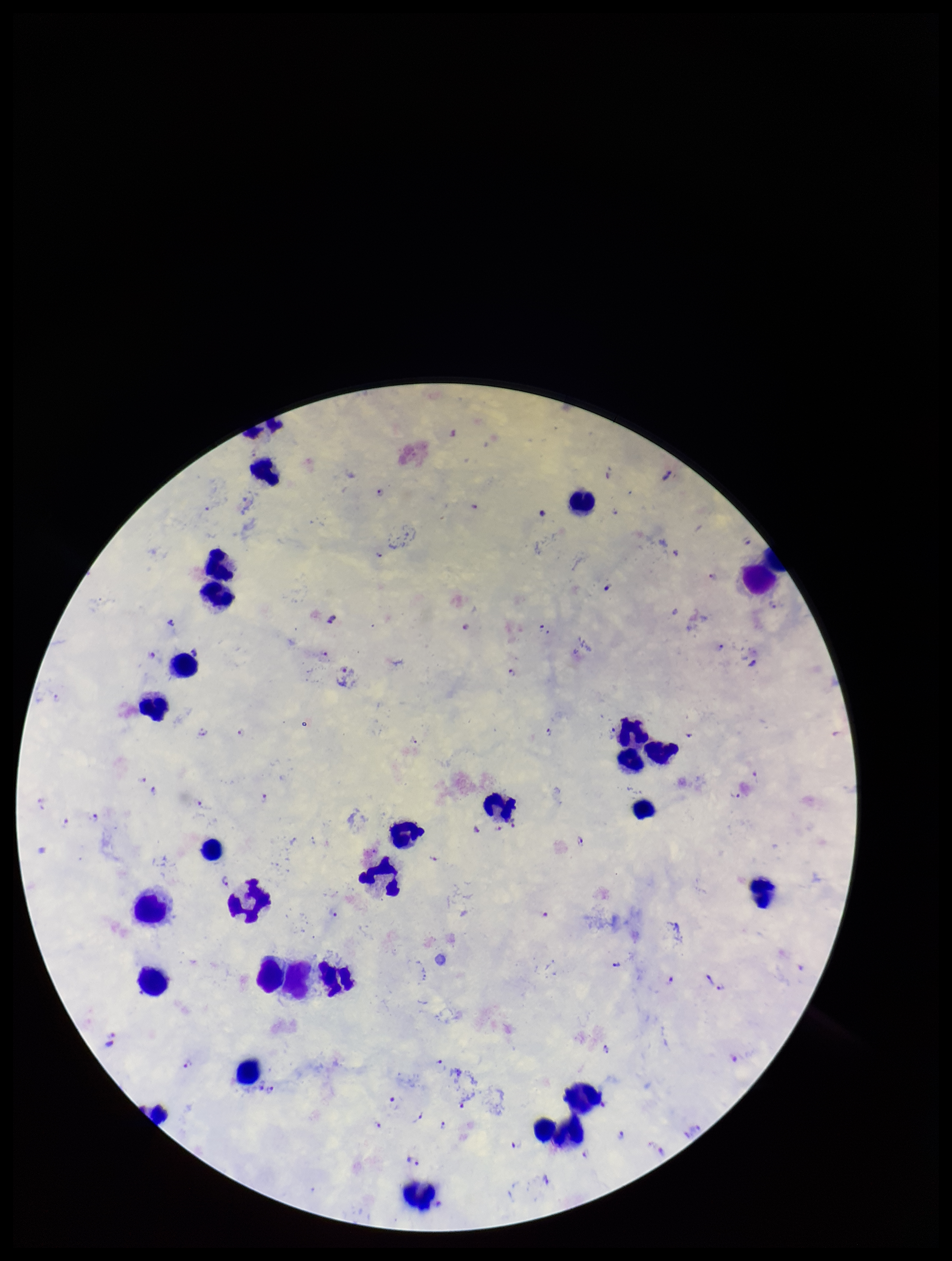
species reported for this patient = Plasmodium falciparum
stain = Giemsa
field of view = single
parasite count = 42
Plasmodium parasites = seen
preparation = thick smear
capture = smartphone photograph through the microscope eyepiece
image size = 952×1261 pixels
leukocyte count = 26
patient malaria status = positive